Locate every Plasmodium falciparum-infected red blood cell.
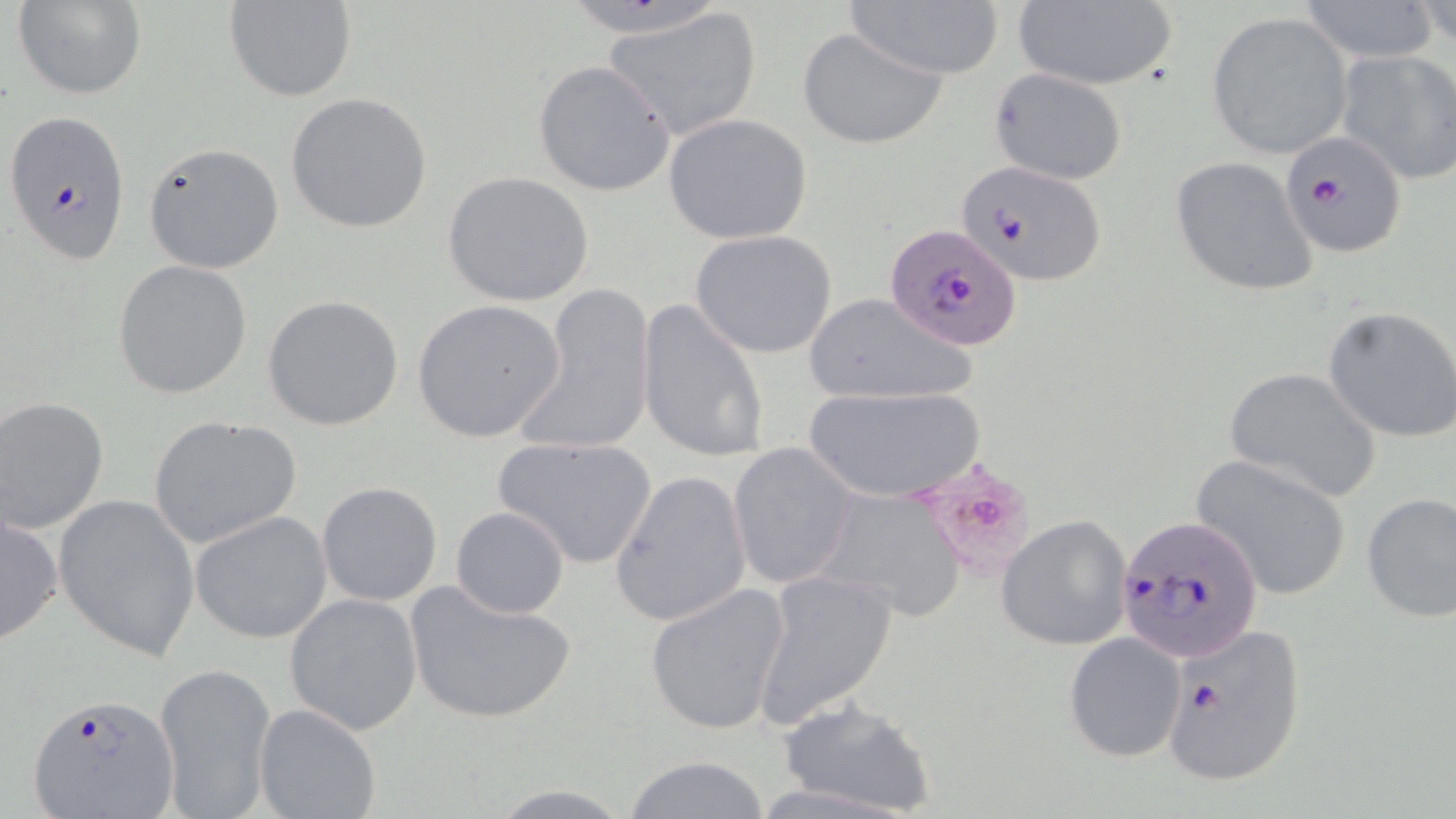

Approximate bounding boxes as (x1, y1, x2, y2) in pixels.
Plasmodium falciparum-infected red blood cells: (4, 109, 131, 265), (1279, 131, 1407, 257), (957, 159, 1106, 285), (879, 226, 1018, 353), (1114, 515, 1265, 663), (1161, 622, 1308, 787), (25, 692, 180, 817).

slide-level diagnosis = Plasmodium falciparum
magnification = 1000x
preparation = thin blood smear
field of view = one of a larger specimen
uninfected red blood cell locations = approximate bounding boxes as (x1, y1, x2, y2) in pixels: (12, 0, 146, 100), (1010, 0, 1182, 91), (1295, 0, 1439, 61), (225, 1, 356, 102), (843, 3, 1005, 80), (604, 7, 763, 141), (1207, 13, 1353, 158), (798, 26, 948, 150), (1333, 47, 1456, 187), (532, 60, 676, 197), (988, 68, 1130, 186), (285, 93, 433, 233), (663, 113, 812, 243), (142, 142, 285, 274), (1168, 156, 1319, 298), (441, 171, 595, 307), (689, 229, 840, 360), (113, 260, 256, 399), (519, 284, 657, 459), (261, 294, 406, 432), (802, 294, 979, 407), (410, 298, 567, 443), (636, 298, 771, 464), (1323, 305, 1456, 443), (1223, 367, 1381, 503), (803, 384, 987, 505), (1, 396, 109, 534), (147, 415, 303, 550), (492, 435, 657, 570), (728, 441, 858, 591), (1189, 454, 1354, 601), (611, 469, 752, 627), (316, 482, 443, 607), (808, 486, 970, 625), (53, 492, 201, 661), (1360, 492, 1456, 623), (451, 506, 570, 619), (190, 510, 333, 644), (1, 511, 64, 646), (995, 514, 1134, 651), (751, 567, 899, 731), (405, 580, 578, 725), (643, 584, 791, 735), (282, 592, 425, 734), (1063, 632, 1186, 763), (153, 660, 277, 819), (775, 698, 937, 819), (254, 702, 382, 819), (621, 756, 777, 817), (482, 784, 637, 817)
stain = May-Grünwald-Giemsa
modality = light microscopy
image size = 1456×819 pixels